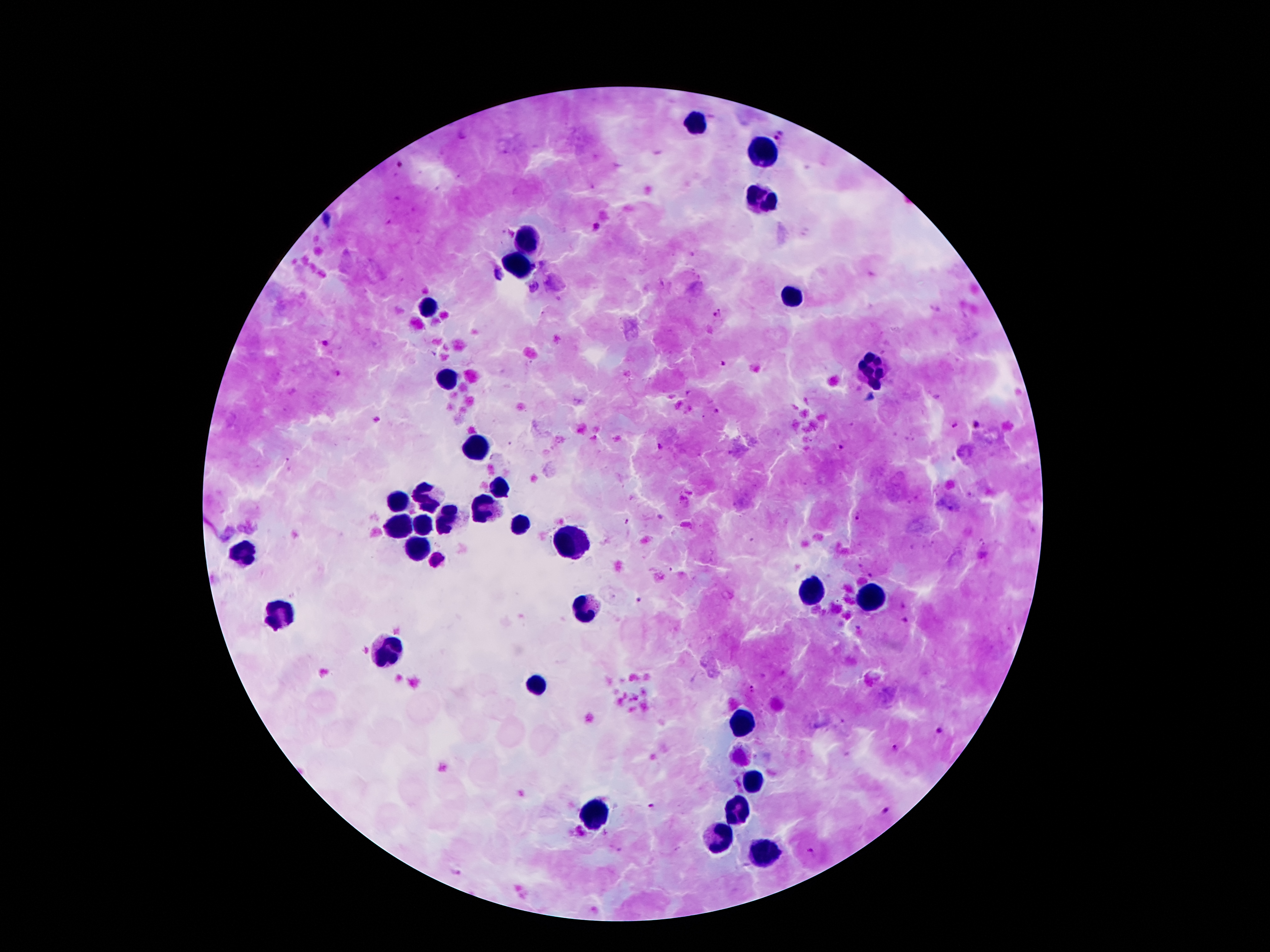
patient_malaria_status: infected with Plasmodium falciparum
field_of_view: single
capture: smartphone through the microscope eyepiece
malaria_parasite_locations: 'approximate centers as [x, y] in pixels: [779, 135], [401, 164], [596, 226], [717, 314], [325, 343], [722, 363], [716, 408], [377, 418], [976, 425], [953, 426], [659, 447], [841, 448], [288, 460], [855, 518], [627, 521], [436, 560], [637, 600], [907, 621], [751, 687], [939, 730], [895, 749], [650, 805], [885, 809], [809, 852]'
preparation: thick peripheral-blood smear
image_size: 1270×952 pixels
stain: Giemsa
leukocyte_locations: 'approximate centers as [x, y] in pixels: [696, 123], [761, 152], [761, 200], [527, 241], [518, 270], [793, 294], [430, 308], [872, 375], [452, 382], [473, 448], [498, 483], [425, 493], [396, 504], [480, 509], [448, 516], [423, 524], [398, 525], [521, 525], [569, 539], [419, 548], [242, 554], [812, 593], [871, 600], [584, 607], [282, 611], [385, 654], [537, 687], [739, 725], [754, 786], [739, 813], [594, 814], [716, 835], [762, 854]'
magnification: 100x